Point out each malaria parasite.
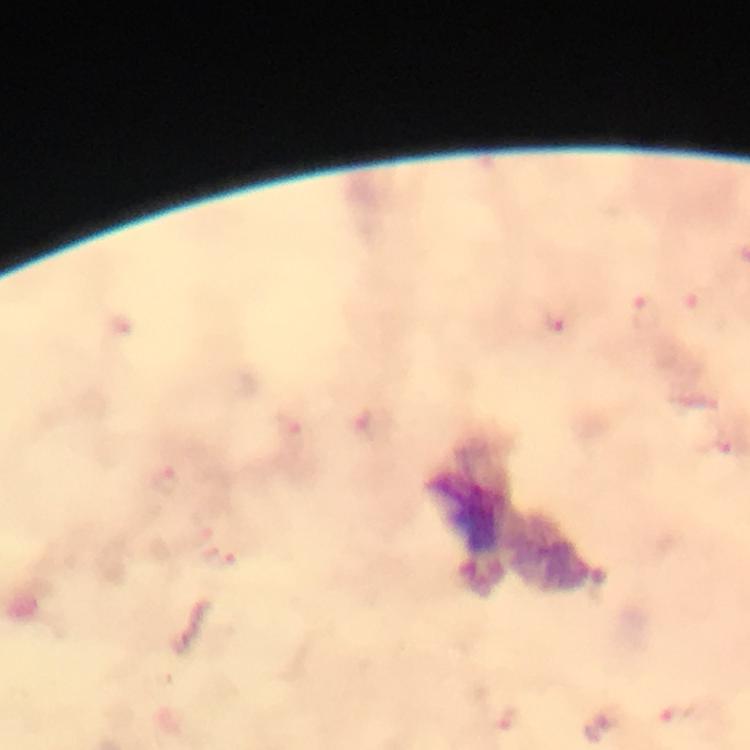

Approximate centers as (x, y) in pixels.
Malaria parasites: (559, 322), (727, 444).

image size = 750×750 pixels
capture = smartphone photograph through a microscope
preparation = thick blood film
magnification = 100x
stain = Giemsa
immersion oil = used
cropped from = one field of view
context = from a diagnostic examination for malaria